Name the cell type shown.
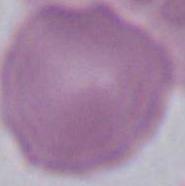

An erythrocyte.

Micrograph. 1000x magnification.